State which parasite is depicted.
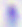

This is Toxoplasma gondii.

Summary:
  - Magnification: 400x
  - Modality: micrograph